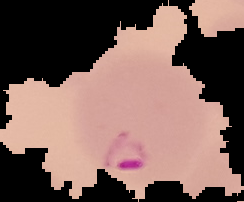
Malaria status: parasitized. Image is 244×202 pixels. From a thin blood smear. The area outside the segmented cell region is set to black.